Report the malaria status of this cell.
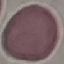
It is uninfected.

Summary:
  - Preparation: thin blood film
  - Stain: Giemsa
  - Capture: smartphone through the microscope eyepiece
  - Image type: cell patch, automatically extracted from a larger field of view and resized to 64 × 64 pixels